Assess the morphology of the red blood cells.
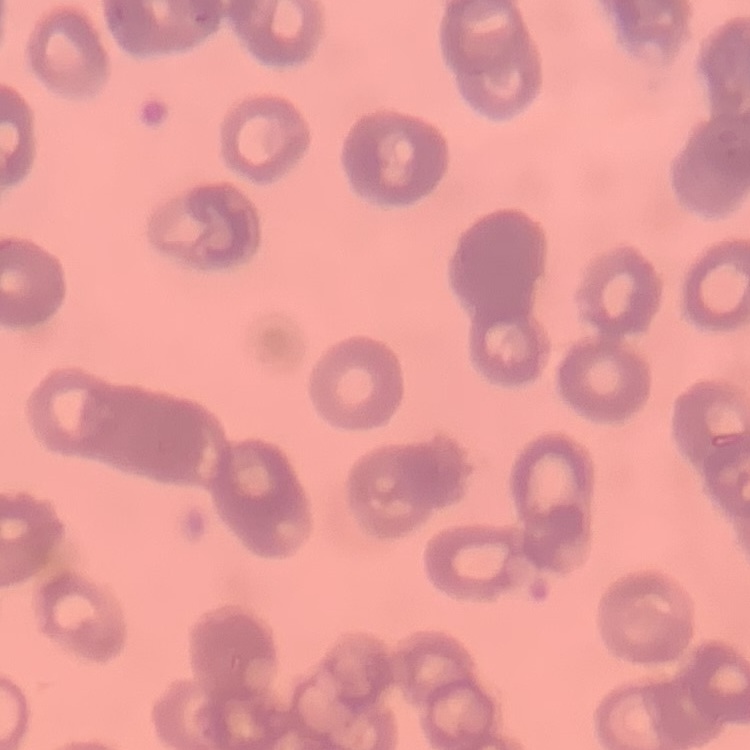

They show rouleaux formation.

preparation: thin peripheral smear
image_type: one tile cut from a larger photomicrograph
stain: Field's or Giemsa